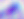

{
  "magnification": "400x",
  "identification": "Toxoplasma gondii",
  "modality": "photomicrograph"
}